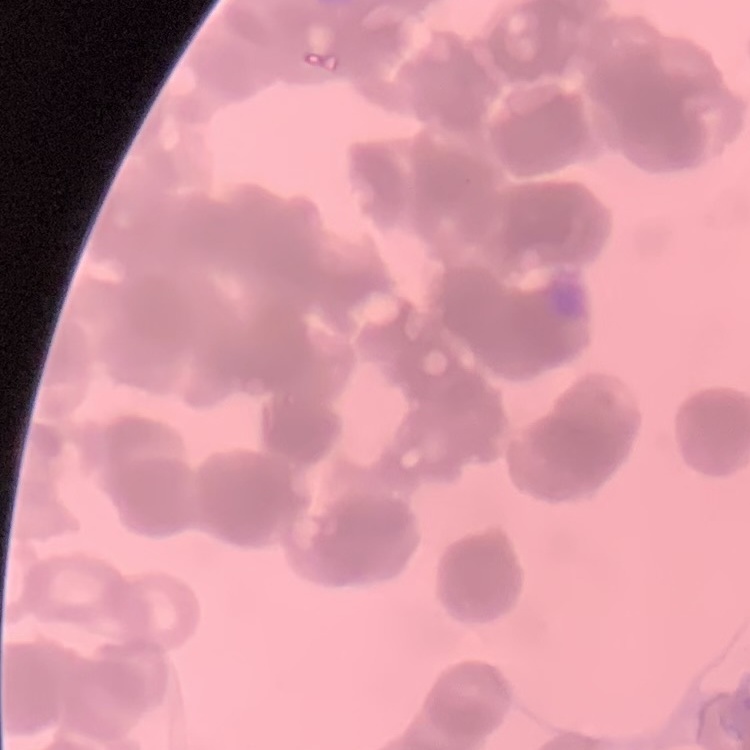

Summary:
  - Erythrocyte morphology: rouleaux formation
  - Preparation: thin blood smear
  - Image type: square crop of a larger photomicrograph
  - Stain: Field's or Giemsa